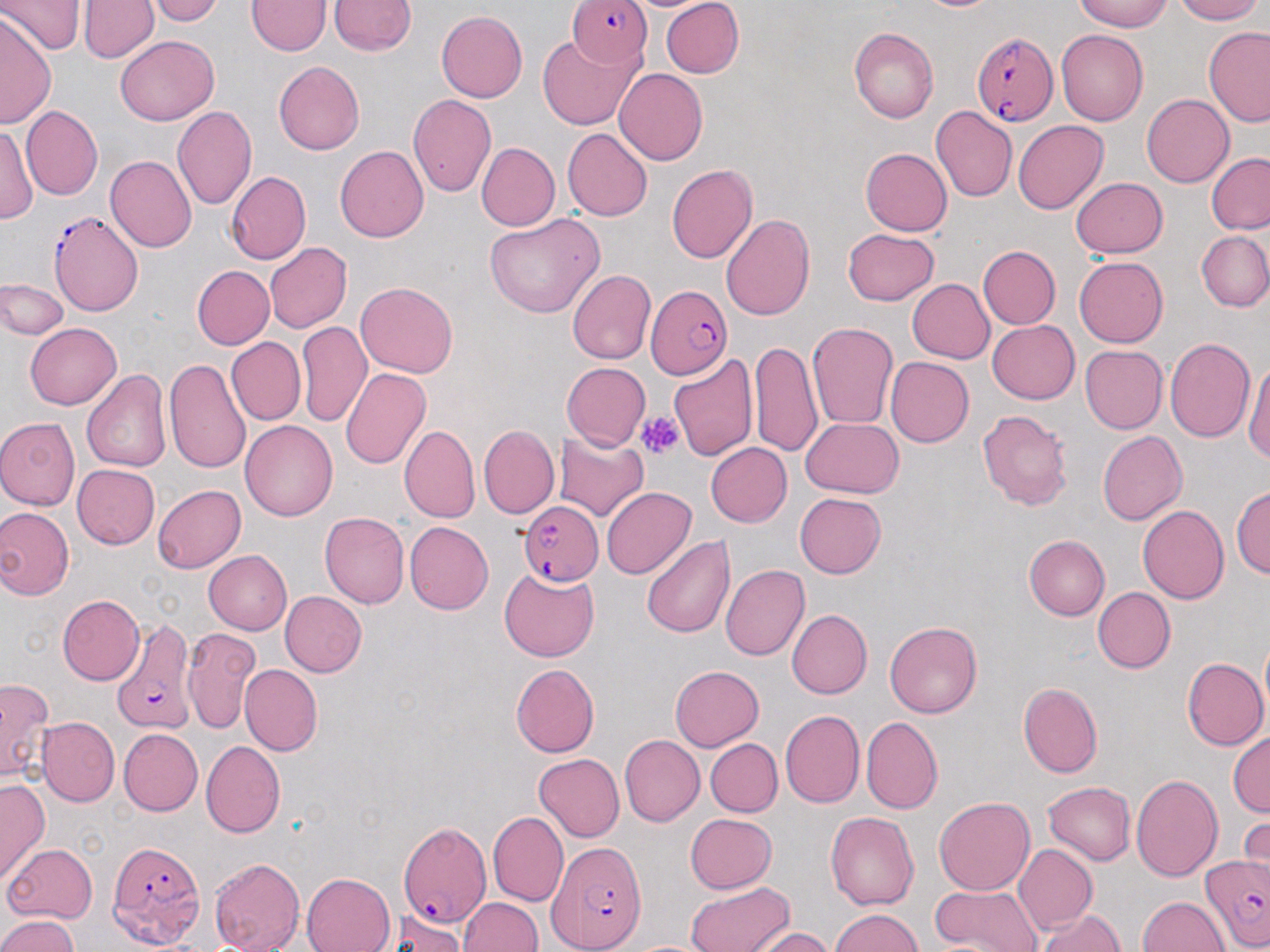

Summary:
  - Coordinate format: approximate bounding boxes as (x1, y1, x2, y2) in pixels
  - Plasmodium falciparum-infected red blood cell locations: (568, 0, 655, 69), (974, 32, 1057, 128), (50, 211, 146, 315), (645, 284, 732, 378), (521, 500, 604, 585), (114, 622, 197, 732), (397, 820, 491, 927), (104, 839, 203, 944), (543, 840, 649, 952), (1201, 856, 1269, 952)
  - Uninfected red blood cell locations: (3, 0, 81, 55), (80, 0, 158, 64), (150, 0, 223, 24), (329, 0, 415, 57), (660, 0, 746, 77), (910, 0, 1010, 15), (1070, 0, 1180, 31), (1170, 0, 1267, 24), (248, 1, 327, 56), (436, 10, 527, 103), (0, 13, 57, 128), (849, 26, 940, 125), (1202, 26, 1270, 127), (1056, 29, 1148, 125), (117, 36, 218, 124), (537, 38, 640, 130), (273, 61, 366, 154), (612, 69, 707, 166), (406, 92, 496, 198), (1140, 94, 1232, 188), (171, 105, 257, 211), (22, 107, 103, 199), (931, 107, 1017, 203), (1013, 120, 1107, 215), (1, 125, 38, 224), (563, 129, 652, 219), (475, 142, 558, 232), (335, 144, 432, 242), (861, 147, 953, 236), (1207, 153, 1270, 236), (105, 154, 196, 254), (667, 164, 757, 266), (225, 171, 310, 264), (1070, 176, 1166, 258), (721, 211, 816, 322), (484, 214, 605, 321), (841, 228, 940, 305), (1196, 230, 1270, 312), (264, 240, 351, 333), (979, 246, 1060, 328), (1073, 254, 1168, 345), (191, 266, 274, 349), (566, 269, 654, 365), (906, 277, 994, 363), (1, 281, 69, 340), (355, 282, 458, 379), (297, 319, 370, 425), (988, 320, 1081, 404), (26, 321, 122, 409), (806, 322, 898, 432), (1165, 336, 1255, 444), (226, 338, 305, 425), (750, 339, 825, 458), (1079, 345, 1166, 433), (666, 349, 757, 462), (885, 357, 972, 448), (1243, 359, 1270, 473), (164, 360, 250, 475), (564, 362, 651, 450), (83, 367, 176, 473), (341, 369, 431, 470), (975, 408, 1072, 508), (0, 417, 80, 509), (800, 417, 903, 499), (242, 421, 337, 522), (399, 426, 478, 524), (477, 426, 558, 519), (555, 428, 648, 523), (1097, 429, 1189, 525), (708, 443, 792, 527), (73, 464, 159, 550), (153, 483, 246, 571), (1233, 485, 1269, 583), (601, 487, 694, 580), (795, 493, 887, 579), (1136, 504, 1229, 604), (0, 507, 73, 600), (320, 511, 409, 608), (405, 522, 493, 614), (642, 532, 734, 638), (1026, 536, 1110, 619), (204, 551, 291, 634), (721, 563, 809, 662), (499, 568, 597, 661), (1092, 587, 1175, 674), (279, 591, 366, 677), (57, 594, 146, 686), (789, 610, 872, 698), (191, 617, 272, 806), (885, 621, 982, 718), (182, 628, 259, 732), (1182, 658, 1267, 748), (239, 663, 322, 756), (511, 664, 598, 757), (669, 665, 763, 752), (0, 678, 54, 780), (1018, 683, 1103, 777), (778, 710, 863, 810), (861, 717, 941, 813), (38, 718, 118, 805), (121, 728, 205, 815), (1228, 731, 1270, 818), (620, 734, 705, 827), (705, 737, 781, 816), (201, 742, 285, 838), (535, 752, 625, 840), (1131, 774, 1224, 883), (1043, 779, 1136, 864), (0, 782, 49, 877), (933, 796, 1034, 896), (824, 809, 919, 908), (488, 812, 568, 903), (683, 812, 776, 894), (1237, 817, 1270, 872), (1, 842, 97, 926), (1013, 845, 1097, 933), (207, 854, 305, 952), (302, 872, 393, 952), (682, 879, 792, 952), (927, 882, 1041, 952), (1138, 895, 1229, 952), (459, 896, 542, 952), (1035, 909, 1128, 952), (828, 910, 927, 952), (390, 914, 468, 950), (0, 915, 81, 952), (752, 926, 837, 952)
  - Platelet locations: (639, 413, 682, 459)
  - Slide-level diagnosis: Plasmodium falciparum
  - Preparation: thin blood smear
  - Image size: 1270×952 pixels
  - Stain: May-Grünwald-Giemsa
  - Magnification: 1000x
  - Modality: optical microscopy
  - Field of view: single